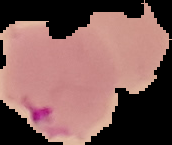
image type = segmented cell region on a black background
image size = 172×145 pixels
result = malaria parasites identified
preparation = thin blood smear